Identify the preparation type.
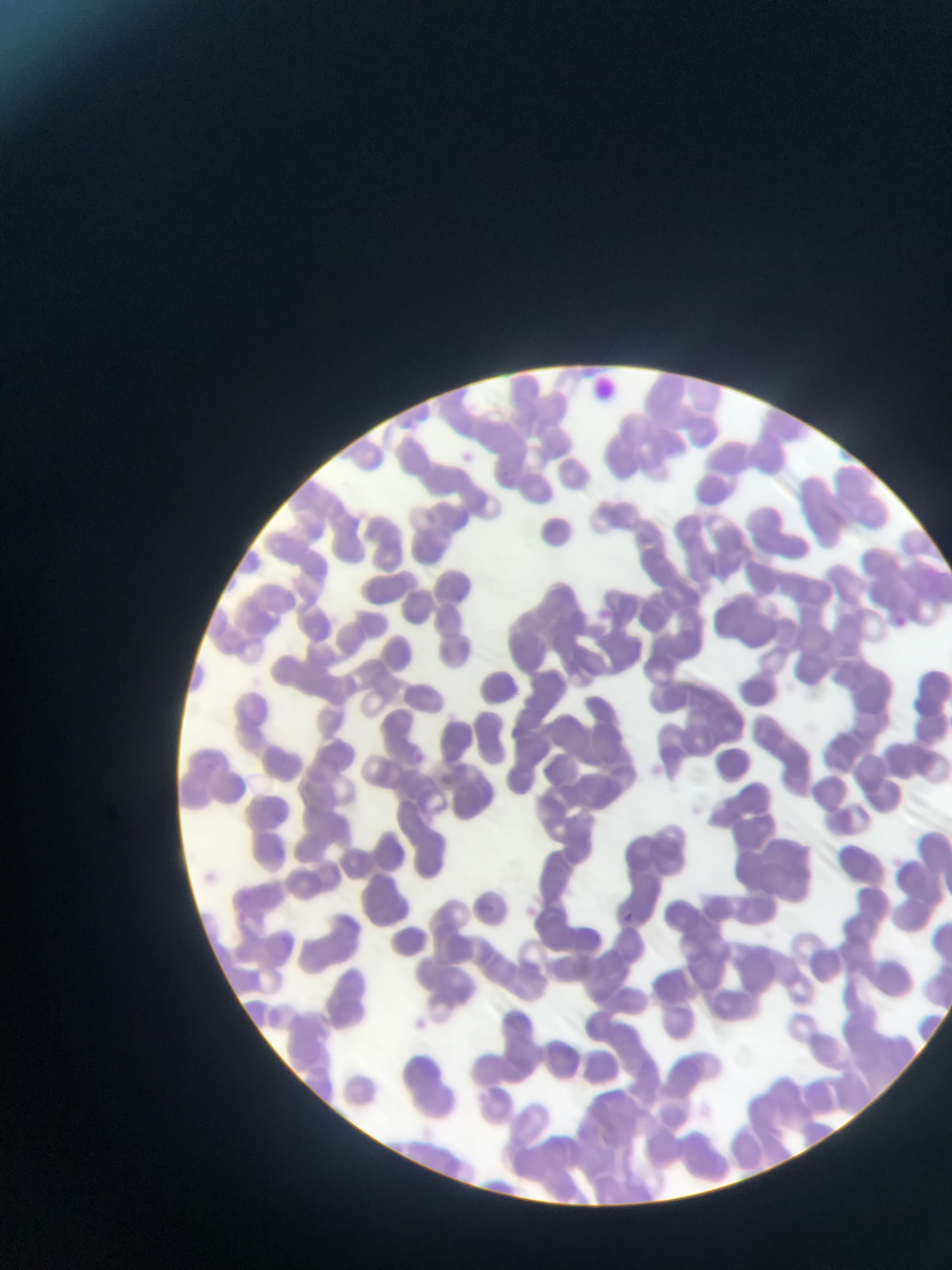
This is a thin smear.

capture = mobile-phone photograph through a microscope
image size = 952×1270 pixels
country = Ghana
field of view = single
malaria parasite locations = approximate bounding boxes as left top right bottom in pixels: 595 605 614 622; 891 614 909 630; 611 908 638 930